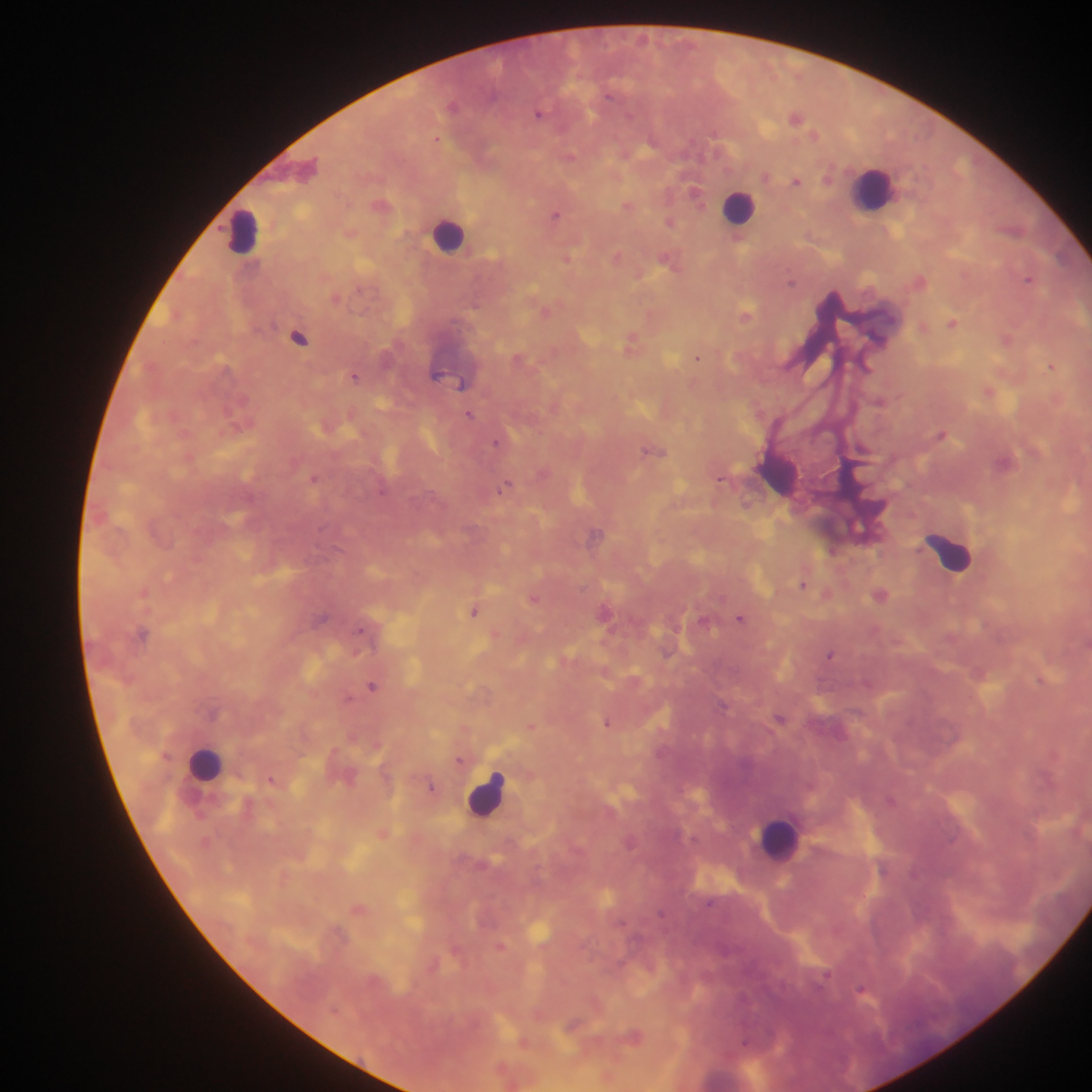
Approximate centers as (x, y) in pixels.
Summary:
  - Leukocyte locations: (875, 191), (744, 203), (252, 224), (450, 240), (945, 554), (202, 766), (492, 798), (779, 835)
  - Malaria parasite locations: (538, 115), (797, 118), (815, 135), (695, 194), (555, 215), (671, 221), (809, 235), (618, 256), (567, 260), (920, 280), (1028, 280), (794, 283), (337, 297), (649, 314), (747, 314), (952, 322), (299, 337), (632, 339), (1007, 339), (700, 358), (1051, 365), (868, 367), (460, 382), (989, 391), (880, 401), (470, 413), (943, 433), (496, 442), (721, 478), (315, 479), (508, 483), (502, 487), (802, 584), (144, 591), (535, 597), (475, 611), (321, 618), (740, 618), (362, 630), (830, 654), (373, 686), (349, 698), (607, 723), (530, 727), (459, 760), (271, 778), (433, 788), (357, 908), (661, 913), (500, 945), (861, 988), (633, 1035), (523, 1040)
  - Preparation: thick blood smear
  - Image size: 1092×1092 pixels
  - Capture: mobile-phone photograph through a microscope
  - Field of view: single
  - Country: Ghana